Report the malaria status of this cell.
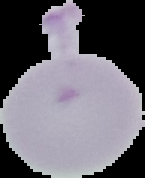
It is uninfected.

The area outside the segmented cell region is set to black. Image is 145×178 pixels. From a thin blood film.